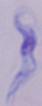
A trypanosome is seen. Photomicrograph. Captured at 1000x magnification.